Describe the morphology of the red blood cells.
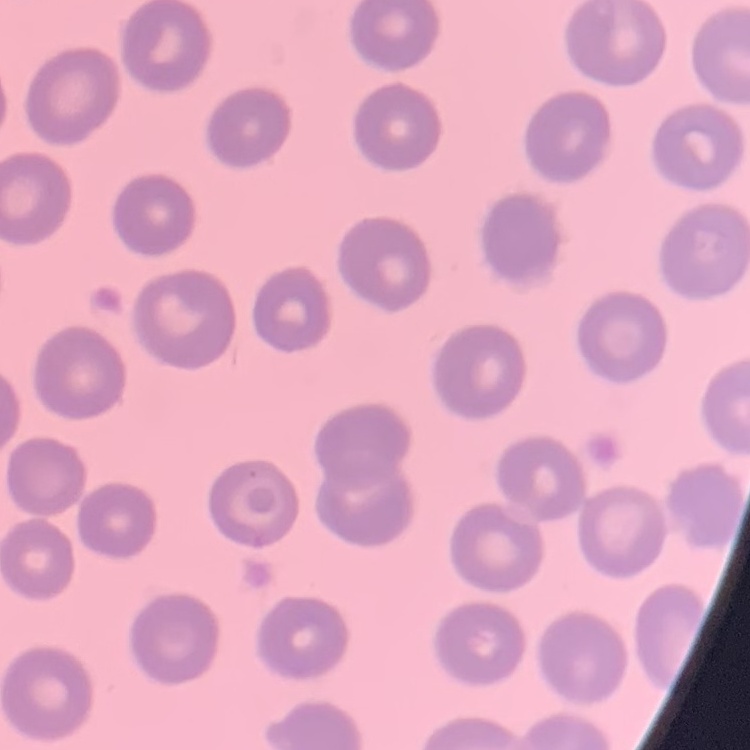

They show no rouleaux formation.

Field's or Giemsa stain. Thin blood film. Square crop of a larger photomicrograph.